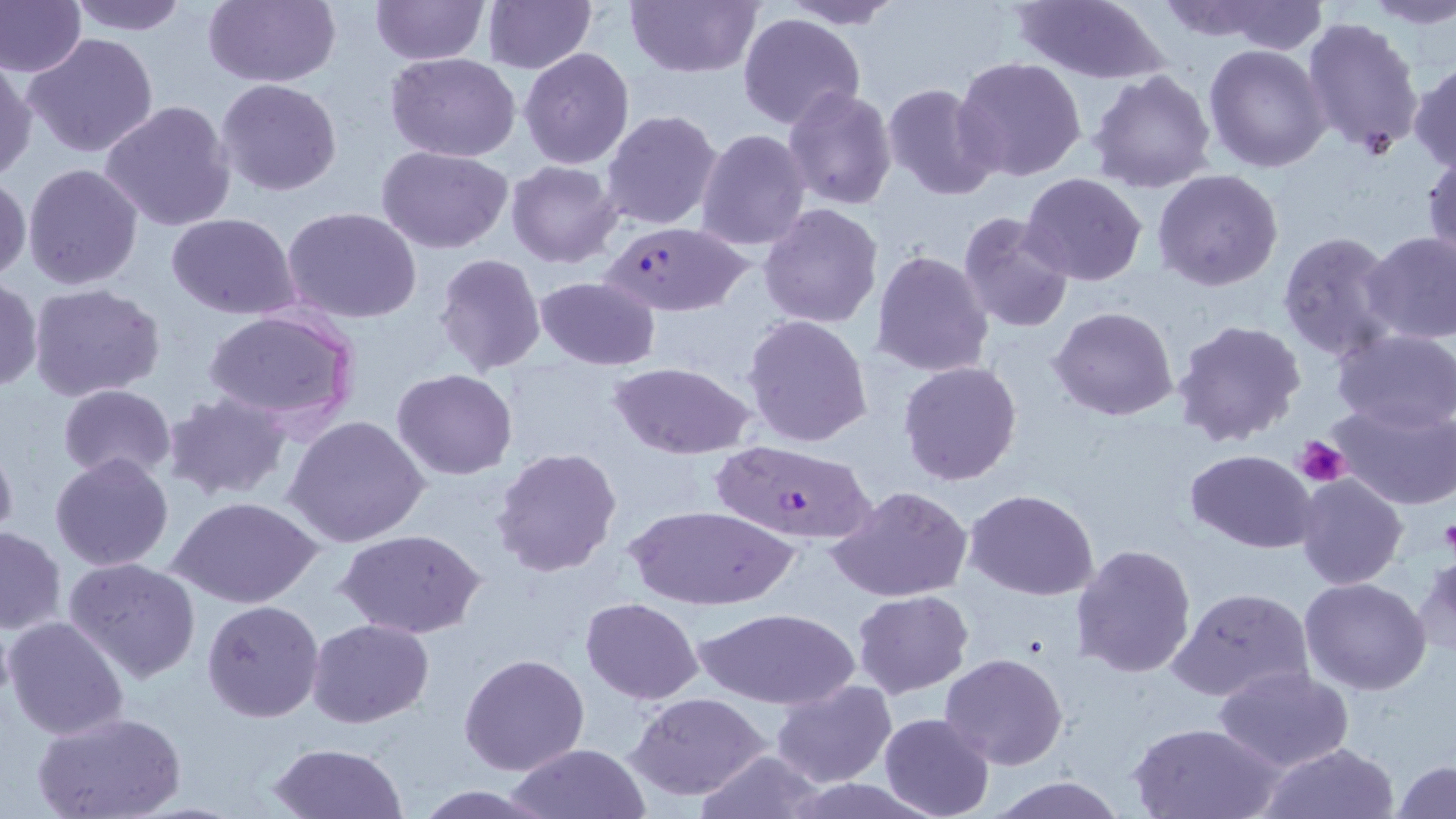
slide_level_diagnosis: Plasmodium falciparum
preparation: thin blood film
plasmodium_falciparum_infected_red_blood_cell_locations: 'approximate bounding boxes as [x1, y1, x2, y2] in pixels: [598, 222, 755, 315], [707, 437, 883, 548]'
stain: May-Grünwald-Giemsa
modality: light microscopy
uninfected_red_blood_cell_locations: 'approximate bounding boxes as [x1, y1, x2, y2] in pixels: [0, 0, 86, 78], [67, 0, 189, 36], [202, 0, 340, 88], [370, 0, 489, 66], [482, 0, 596, 74], [626, 0, 763, 78], [1008, 0, 1170, 83], [1358, 0, 1456, 29], [776, 1, 903, 29], [1213, 3, 1326, 54], [737, 11, 865, 131], [1302, 16, 1424, 155], [23, 31, 161, 161], [1204, 45, 1332, 174], [519, 47, 634, 170], [386, 53, 521, 162], [953, 55, 1088, 181], [0, 58, 37, 183], [1409, 61, 1456, 174], [1087, 67, 1219, 195], [216, 78, 343, 198], [882, 83, 1001, 201], [783, 86, 899, 211], [100, 100, 235, 232], [600, 109, 724, 230], [696, 128, 812, 250], [377, 145, 513, 253], [1422, 149, 1455, 272], [506, 161, 622, 267], [22, 163, 144, 290], [1152, 168, 1284, 291], [0, 170, 30, 285], [1020, 173, 1148, 288], [758, 202, 883, 327], [281, 207, 424, 325], [956, 211, 1073, 334], [167, 213, 300, 320], [1277, 231, 1401, 363], [1363, 231, 1456, 345], [552, 241, 744, 351], [871, 249, 994, 379], [434, 252, 547, 377], [0, 276, 42, 394], [535, 277, 660, 369], [26, 283, 167, 403], [1050, 306, 1179, 422], [200, 308, 359, 428], [743, 314, 874, 449], [1171, 317, 1308, 450], [1330, 327, 1456, 433], [897, 360, 1022, 486], [607, 361, 756, 459], [391, 368, 518, 479], [58, 384, 177, 482], [163, 391, 294, 503], [1329, 401, 1456, 512], [284, 413, 430, 549], [0, 438, 18, 552], [491, 446, 622, 579], [1186, 449, 1317, 552], [49, 452, 176, 572], [1295, 473, 1407, 590], [828, 485, 972, 603], [965, 490, 1097, 600], [170, 494, 322, 609], [629, 504, 797, 610], [1, 525, 65, 634], [339, 530, 482, 640], [1070, 543, 1197, 681], [1412, 552, 1456, 664], [62, 557, 204, 683], [1301, 576, 1432, 695], [1167, 585, 1316, 703], [851, 590, 975, 698], [580, 597, 704, 705], [202, 598, 325, 721], [699, 607, 856, 709], [3, 615, 129, 740], [307, 618, 435, 728], [941, 652, 1069, 771], [459, 653, 588, 776], [1211, 665, 1355, 774], [769, 680, 895, 788], [628, 690, 772, 801], [33, 711, 185, 819], [879, 713, 994, 819], [1128, 721, 1283, 819], [267, 742, 406, 819], [506, 742, 652, 818], [1260, 742, 1398, 819], [693, 750, 827, 819], [1392, 759, 1455, 818], [988, 773, 1128, 818], [410, 784, 555, 818]'
field_of_view: single
image_size: 1456×819 pixels
platelet_locations: 'approximate bounding boxes as [x1, y1, x2, y2] in pixels: [1296, 436, 1350, 488], [1439, 514, 1456, 558]'
magnification: 1000x